Identify the cell.
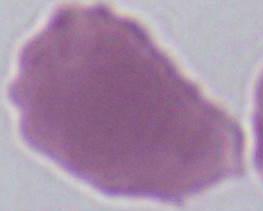
An erythrocyte.

modality = photomicrograph
magnification = 1000x